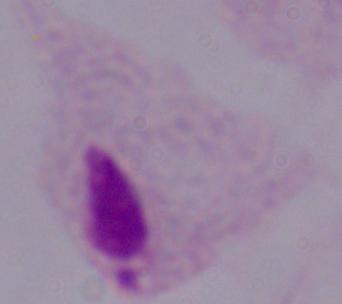
Summary:
  - Identification: trichomonad
  - Modality: micrograph
  - Magnification: 1000x